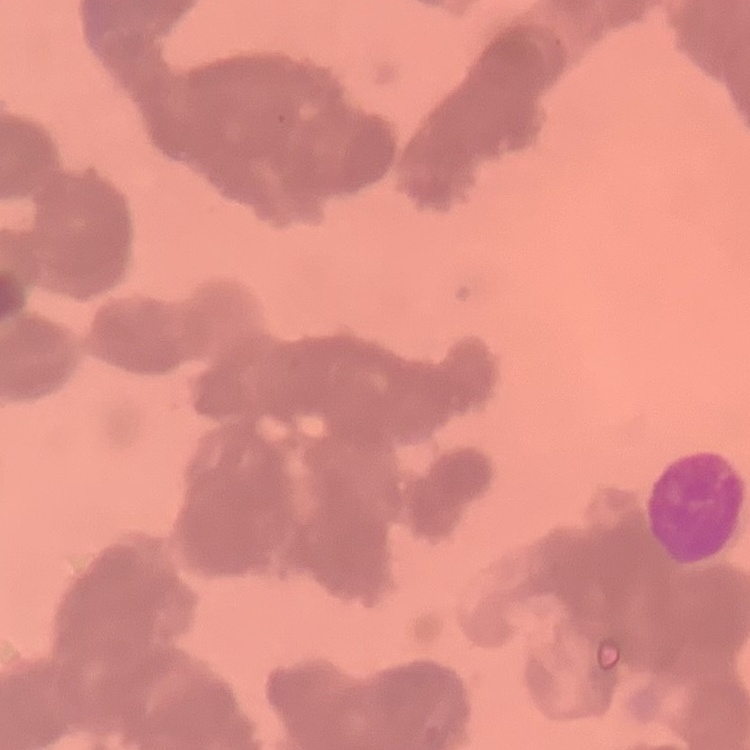

erythrocyte morphology = rouleaux formation
stain = Field's or Giemsa
image type = one tile cut from a larger photomicrograph
preparation = thin peripheral smear